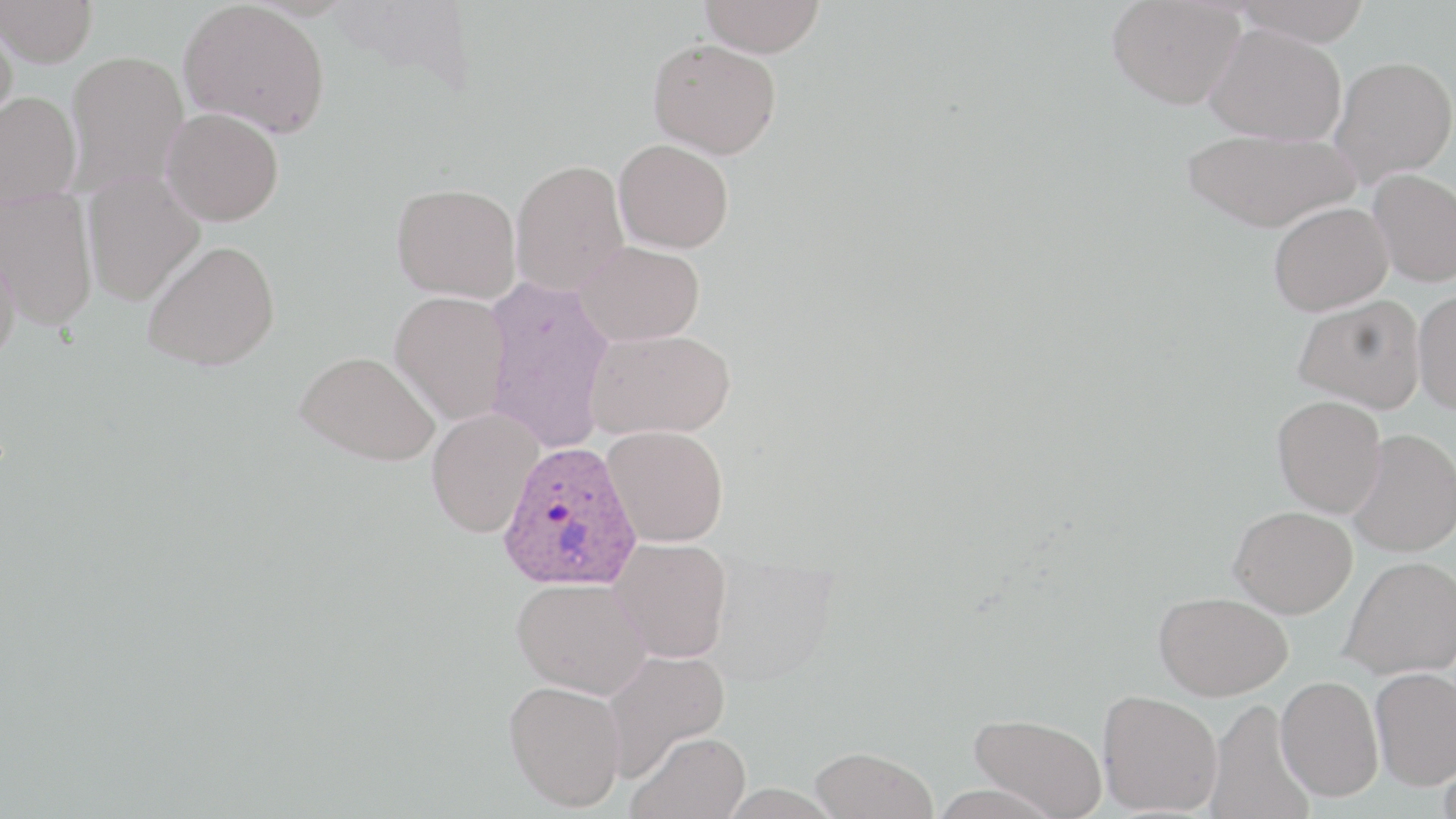
slide-level diagnosis = Plasmodium ovale
field of view = single
stain = May-Grünwald-Giemsa
modality = light microscopy
magnification = 1000x
preparation = thin blood film
uninfected red blood cell locations = approximate bounding boxes as (x1,y1)-(x2,y2) corner pairs in pixels: (699,0)-(826,58), (1107,0)-(1245,109), (1233,0)-(1372,45), (0,1)-(98,68), (178,1)-(331,138), (0,12)-(18,134), (1206,24)-(1347,146), (648,38)-(781,159), (65,50)-(189,193), (1330,55)-(1456,185), (0,91)-(82,207), (161,107)-(284,226), (1182,128)-(1358,232), (613,139)-(734,253), (510,159)-(629,295), (1368,168)-(1456,287), (82,171)-(205,305), (391,182)-(521,302), (0,189)-(98,329), (1268,201)-(1392,315), (0,235)-(22,367), (143,240)-(281,371), (575,241)-(705,345), (482,275)-(614,454), (1413,290)-(1456,414), (390,291)-(512,424), (1293,294)-(1425,413), (586,328)-(735,440), (295,350)-(441,465), (1272,395)-(1387,517), (427,408)-(543,538), (603,425)-(729,547), (1348,429)-(1456,557), (1229,506)-(1357,618), (609,537)-(733,662), (1340,555)-(1456,679), (512,577)-(651,699), (1154,591)-(1292,700), (602,648)-(731,779), (1370,667)-(1456,790), (1275,675)-(1383,801), (504,680)-(626,811), (1098,689)-(1223,815), (1206,697)-(1315,819), (969,713)-(1108,818), (628,730)-(750,819), (810,746)-(938,819), (1438,754)-(1456,819)
image size = 1456×819 pixels
Plasmodium ovale-infected red blood cell locations = approximate bounding boxes as (x1,y1)-(x2,y2) corner pairs in pixels: (497,440)-(642,593)